Describe the morphology of the red blood cells.
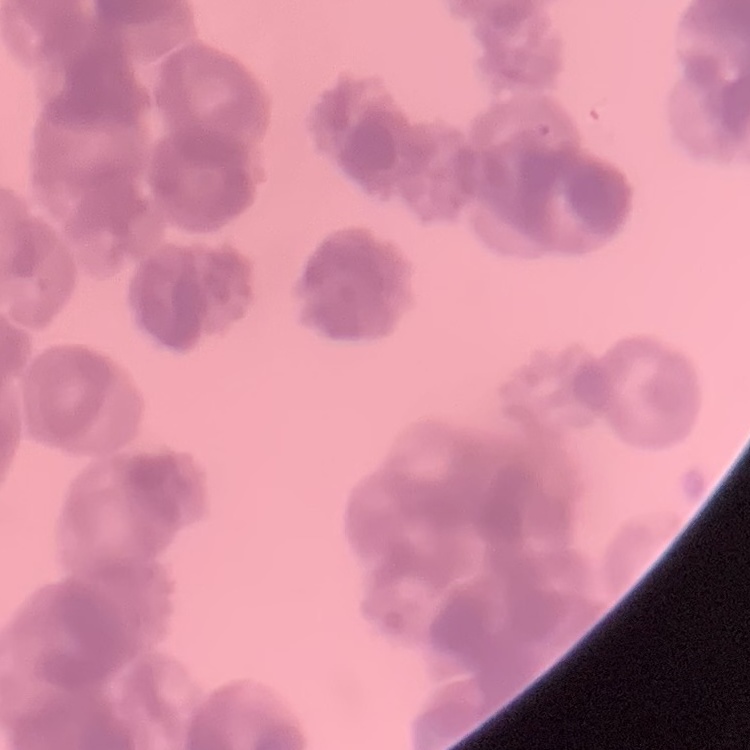

They show rouleaux formation.

{
  "stain": "Field's or Giemsa",
  "image_type": "square crop of a larger photomicrograph",
  "preparation": "thin peripheral smear"
}